State the blood parasite species.
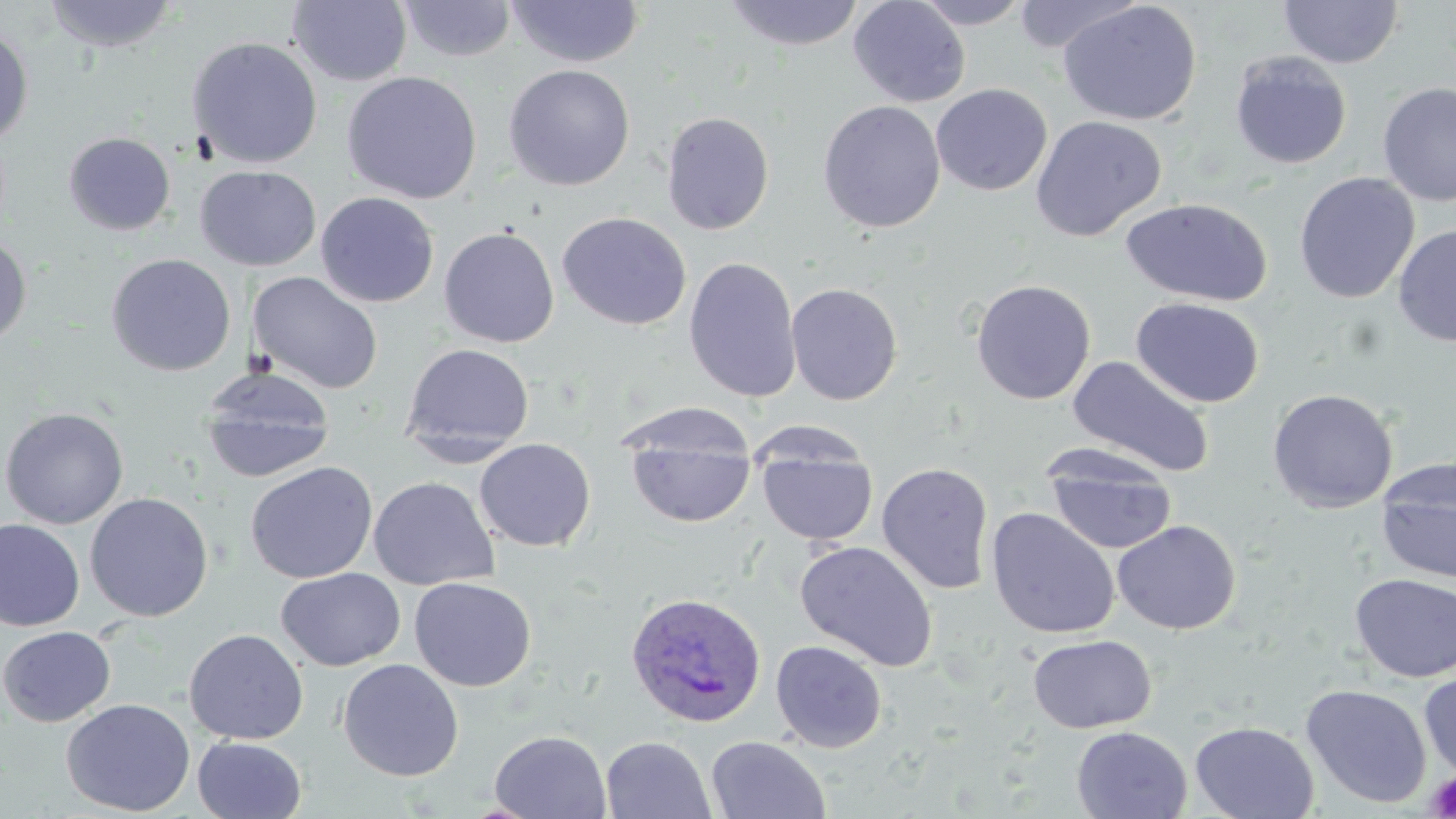
Plasmodium ovale.

field of view = one of a larger specimen
preparation = thin blood smear
stain = May-Grünwald-Giemsa
magnification = 1000x
Plasmodium ovale-infected red blood cell locations = approximate bounding boxes as [x1, y1, x2, y2] in pixels: [624, 591, 767, 729]
image size = 1456×819 pixels
modality = light microscopy
platelet locations = approximate bounding boxes as [x1, y1, x2, y2] in pixels: [1424, 771, 1456, 817]
uninfected red blood cell locations = approximate bounding boxes as [x1, y1, x2, y2] in pixels: [42, 0, 180, 53], [398, 0, 517, 63], [722, 0, 865, 52], [848, 0, 971, 108], [910, 0, 1035, 28], [1008, 0, 1145, 55], [287, 1, 413, 86], [507, 1, 644, 68], [1058, 1, 1202, 126], [1278, 1, 1404, 69], [0, 23, 34, 149], [186, 36, 323, 169], [1229, 51, 1352, 170], [502, 64, 635, 192], [341, 71, 482, 205], [1377, 81, 1456, 207], [930, 82, 1052, 196], [817, 100, 946, 233], [661, 111, 775, 235], [1030, 115, 1167, 242], [63, 132, 176, 236], [195, 165, 321, 271], [1293, 172, 1420, 304], [315, 191, 440, 308], [1120, 197, 1272, 307], [556, 212, 691, 330], [1393, 225, 1456, 346], [438, 226, 560, 348], [0, 234, 32, 346], [105, 253, 237, 377], [683, 256, 803, 403], [247, 271, 383, 394], [970, 278, 1096, 405], [786, 282, 903, 405], [1131, 297, 1265, 408], [400, 343, 534, 456], [1066, 355, 1216, 478], [198, 367, 337, 483], [1266, 388, 1398, 514], [0, 407, 129, 529], [627, 431, 756, 528], [474, 438, 596, 552], [756, 439, 878, 546], [1044, 455, 1178, 555], [245, 461, 378, 583], [1376, 461, 1456, 584], [876, 462, 994, 595], [368, 477, 500, 591], [85, 492, 213, 622], [986, 507, 1121, 640], [0, 518, 85, 631], [1112, 519, 1241, 635], [795, 540, 939, 671], [276, 567, 406, 671], [1349, 573, 1456, 683], [409, 576, 536, 692], [0, 626, 116, 727], [184, 628, 308, 744], [1027, 634, 1158, 733], [770, 640, 889, 754], [337, 659, 464, 782], [1418, 668, 1456, 780], [1300, 683, 1432, 808], [61, 698, 195, 816], [1189, 721, 1319, 819], [1071, 726, 1192, 819], [489, 730, 612, 818], [600, 735, 716, 819], [706, 735, 831, 819], [192, 736, 307, 819]